State which parasite is depicted.
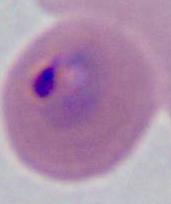
Plasmodium.

modality = micrograph
magnification = 400x or 1000x